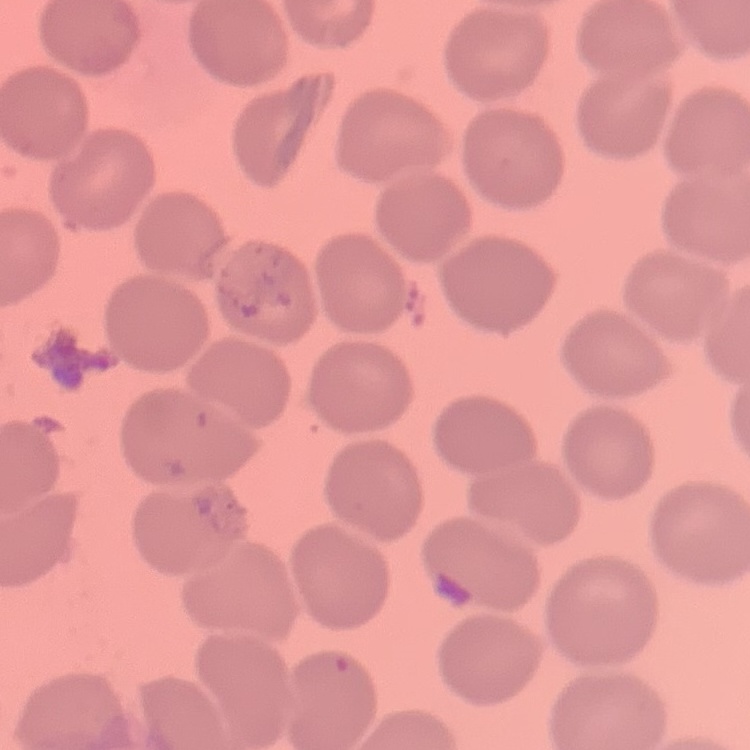

erythrocyte morphology = no rouleaux formation
image type = one tile cut from a larger photomicrograph
preparation = thin peripheral smear
stain = Field's or Giemsa